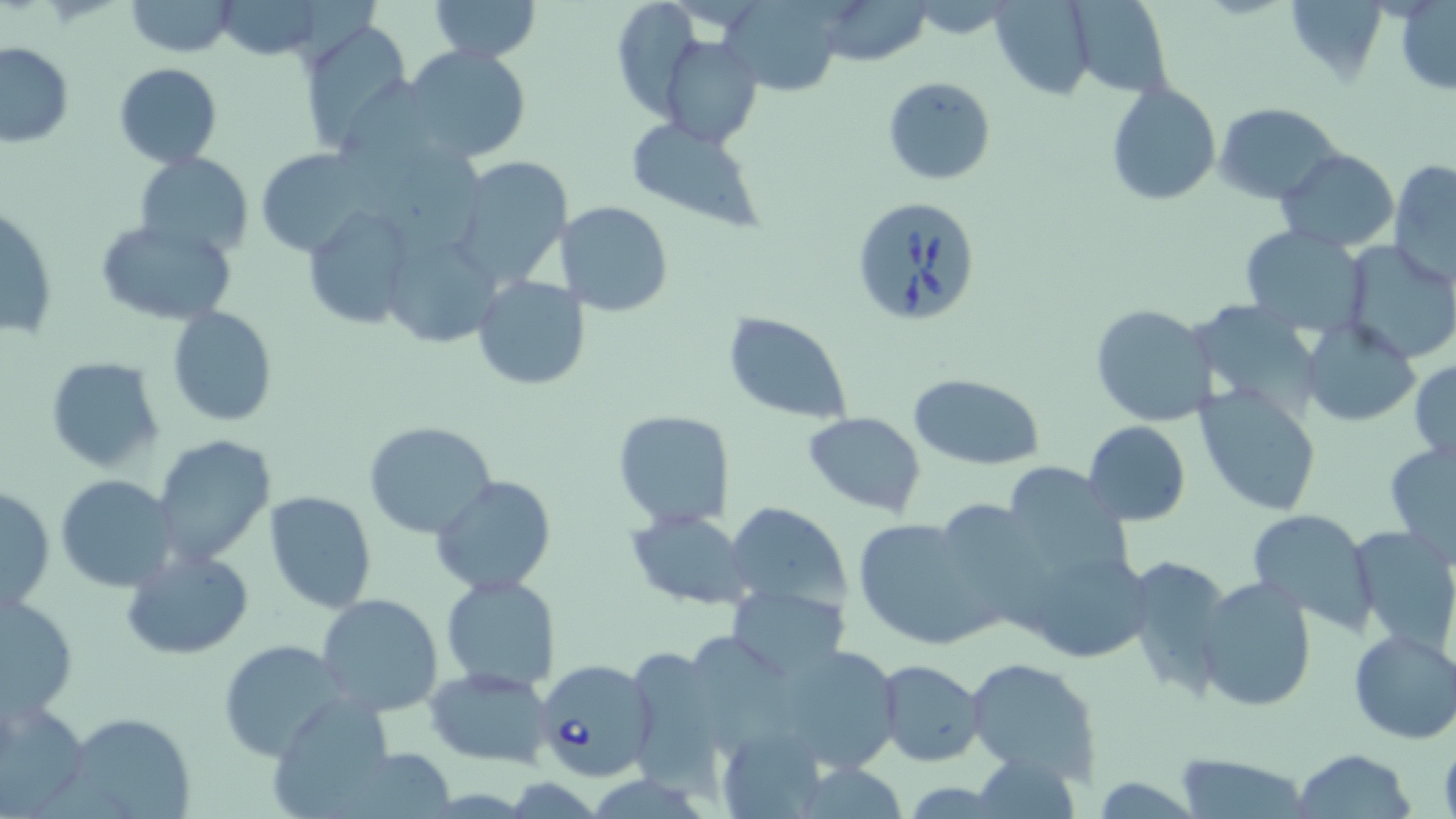

Summary:
  - Coordinate format: approximate bounding boxes as [x1, y1, x2, y2] in pixels
  - Babesia divergens-infected red blood cell locations: [850, 196, 981, 326], [530, 655, 656, 784]
  - Uninfected red blood cell locations: [428, 0, 540, 63], [609, 0, 706, 118], [815, 0, 932, 66], [989, 0, 1096, 99], [123, 1, 238, 56], [719, 1, 845, 95], [1065, 1, 1173, 96], [211, 2, 326, 59], [1395, 2, 1455, 95], [300, 22, 416, 155], [661, 35, 763, 147], [0, 41, 74, 148], [402, 45, 532, 164], [113, 63, 223, 168], [882, 75, 996, 185], [1105, 80, 1221, 206], [1214, 103, 1343, 203], [624, 117, 768, 230], [255, 148, 377, 258], [1276, 148, 1398, 252], [134, 152, 254, 260], [448, 156, 574, 287], [1388, 159, 1456, 288], [558, 200, 672, 317], [1, 207, 58, 343], [305, 208, 415, 332], [94, 218, 238, 328], [1239, 226, 1370, 335], [1337, 240, 1456, 363], [472, 274, 590, 391], [1089, 303, 1217, 428], [167, 306, 278, 426], [722, 312, 853, 424], [1301, 318, 1421, 427], [44, 356, 165, 473], [1409, 360, 1456, 466], [906, 372, 1046, 470], [1194, 384, 1323, 516], [611, 410, 735, 529], [802, 411, 927, 518], [364, 420, 497, 539], [1083, 420, 1190, 525], [150, 434, 275, 567], [1384, 440, 1456, 567], [998, 460, 1132, 580], [432, 474, 555, 597], [56, 475, 180, 591], [1, 486, 54, 612], [264, 491, 376, 612], [928, 498, 1056, 627], [724, 501, 853, 616], [1246, 508, 1380, 631], [627, 510, 753, 610], [852, 517, 1001, 649], [1347, 526, 1456, 658], [1018, 544, 1154, 664], [121, 546, 256, 661], [1123, 555, 1233, 699], [439, 574, 562, 693], [1196, 576, 1317, 713], [727, 582, 850, 678], [1, 591, 78, 721], [317, 593, 442, 716], [1347, 628, 1456, 744], [218, 638, 345, 761], [766, 643, 905, 773], [620, 645, 734, 790], [965, 656, 1101, 784], [877, 659, 987, 767], [426, 667, 554, 768], [1, 698, 89, 813], [269, 703, 408, 810], [65, 712, 197, 819], [716, 724, 832, 817], [1292, 748, 1417, 819], [971, 749, 1079, 819], [1174, 755, 1316, 817]
  - Slide-level diagnosis: Babesia divergens
  - Field of view: single
  - Image size: 1456×819 pixels
  - Preparation: thin blood smear
  - Magnification: 1000x
  - Stain: May-Grünwald-Giemsa
  - Modality: light microscopy